Assess the morphology of the erythrocytes.
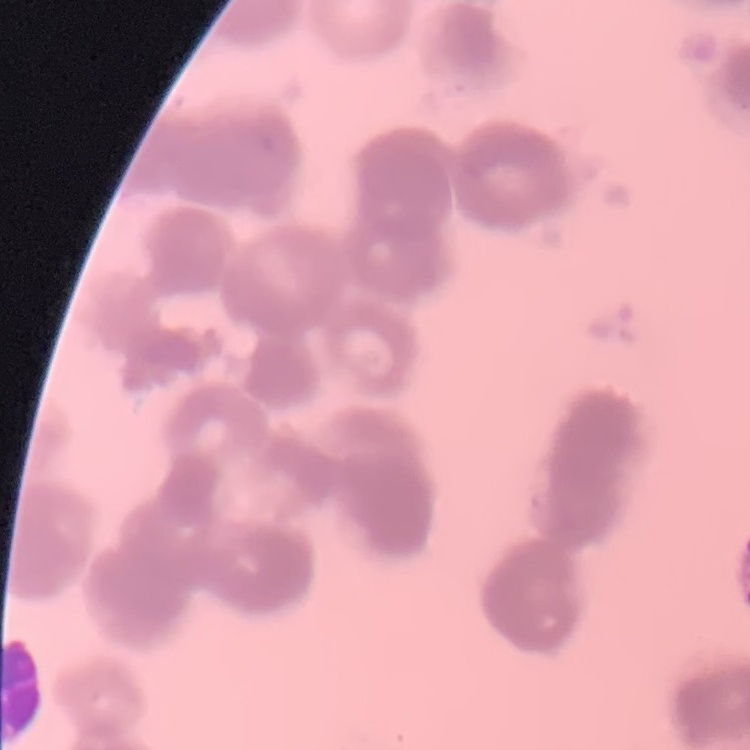
They show rouleaux formation.

Summary:
  - Image type: one tile cut from a larger photomicrograph
  - Preparation: thin blood film
  - Stain: Field's or Giemsa